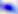
Summary:
  - Modality: photomicrograph
  - Identification: Toxoplasma gondii
  - Magnification: 400x